Describe the morphology of the erythrocytes.
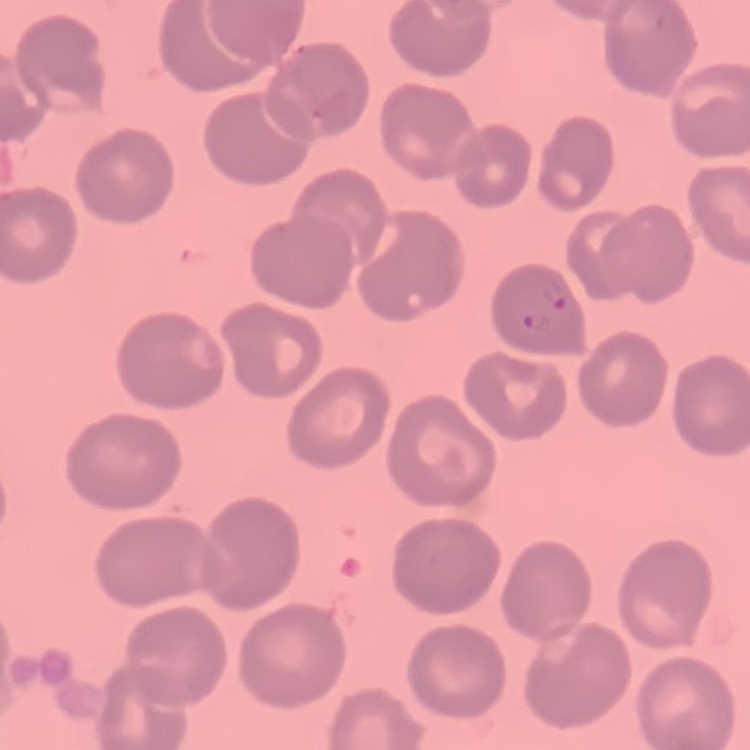

No rouleaux formation.

Field's or Giemsa stain. Square crop of a larger photomicrograph. Thin blood smear.